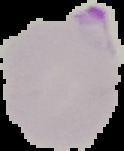

{
  "image_type": "cell region segmented out of the field of view; surrounding area masked to black",
  "malaria_status": "parasitized",
  "preparation": "thin blood film",
  "image_size": "124×151 pixels"
}